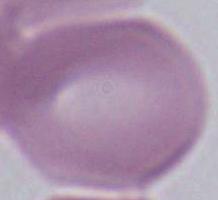
Summary:
  - Identification: red blood cell
  - Modality: micrograph
  - Magnification: 1000x